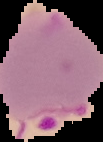
Summary:
  - Image size: 103×142 pixels
  - Preparation: thin blood smear
  - Result: malaria parasites detected
  - Image type: segmented cell region on a black background